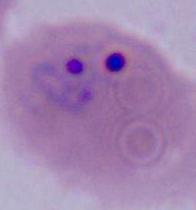 400x or 1000x magnification. A Plasmodium parasite is seen. Photomicrograph.